Classify the preparation.
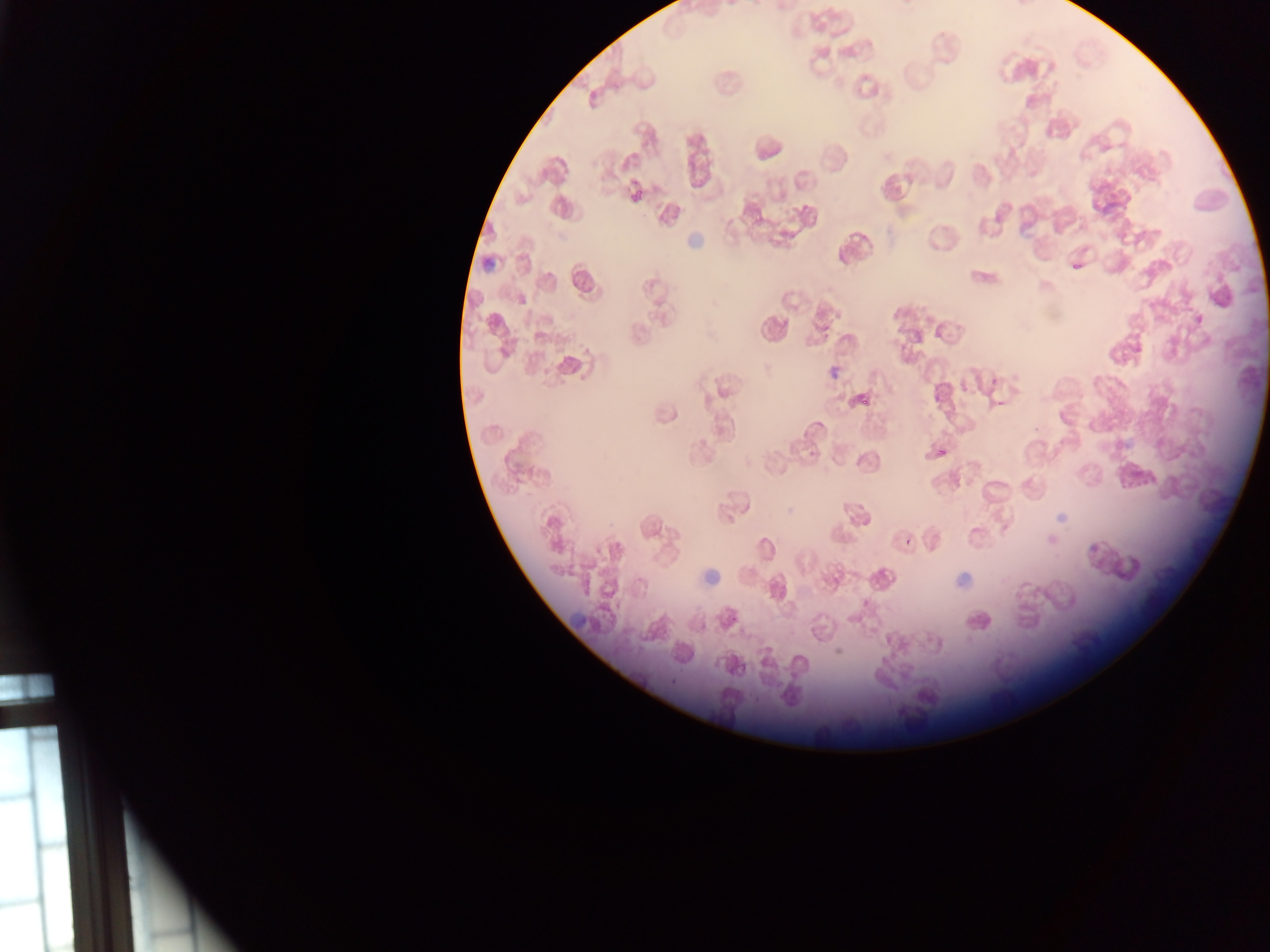
Thin blood film.

Approximate bounding boxes as {left, top, right, bottom} in pixels. Plasmodium parasite locations: {1072, 263, 1080, 270}, {855, 392, 870, 406}, {936, 434, 951, 456}, {904, 538, 913, 546}. Artifact (stain precipitate or debris) locations: {679, 224, 708, 257}, {477, 259, 498, 274}, {1053, 505, 1072, 524}, {703, 565, 722, 584}, {950, 572, 974, 589}, {568, 612, 587, 638}. Mobile-phone photograph taken through the microscope. One field of view. Sample from Ghana. Image is 1270×952 pixels.